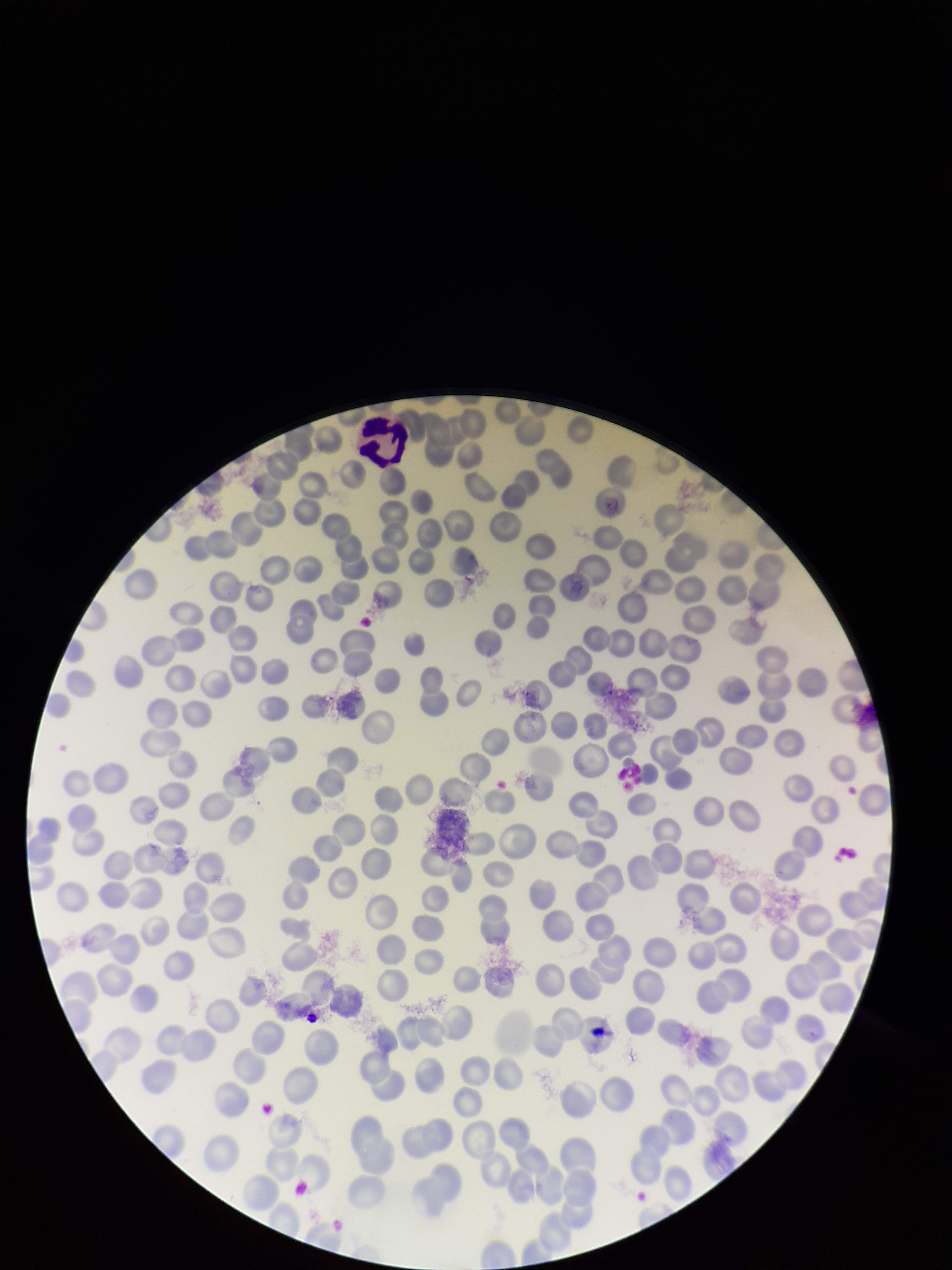 Smartphone photograph taken through the eyepiece of a microscope. Patient malaria status: negative. One field from this slide. Parasitized red blood cell count: 0. Giemsa stain. Parasitized red blood cells: none identified. Red blood cell count: 207. Preparation: thin. Image is 952×1270 pixels.